Name the parasite shown.
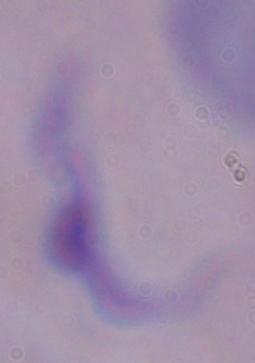

A trypanosome.

magnification: 1000x
modality: photomicrograph